Locate every blood parasite and identify its species.
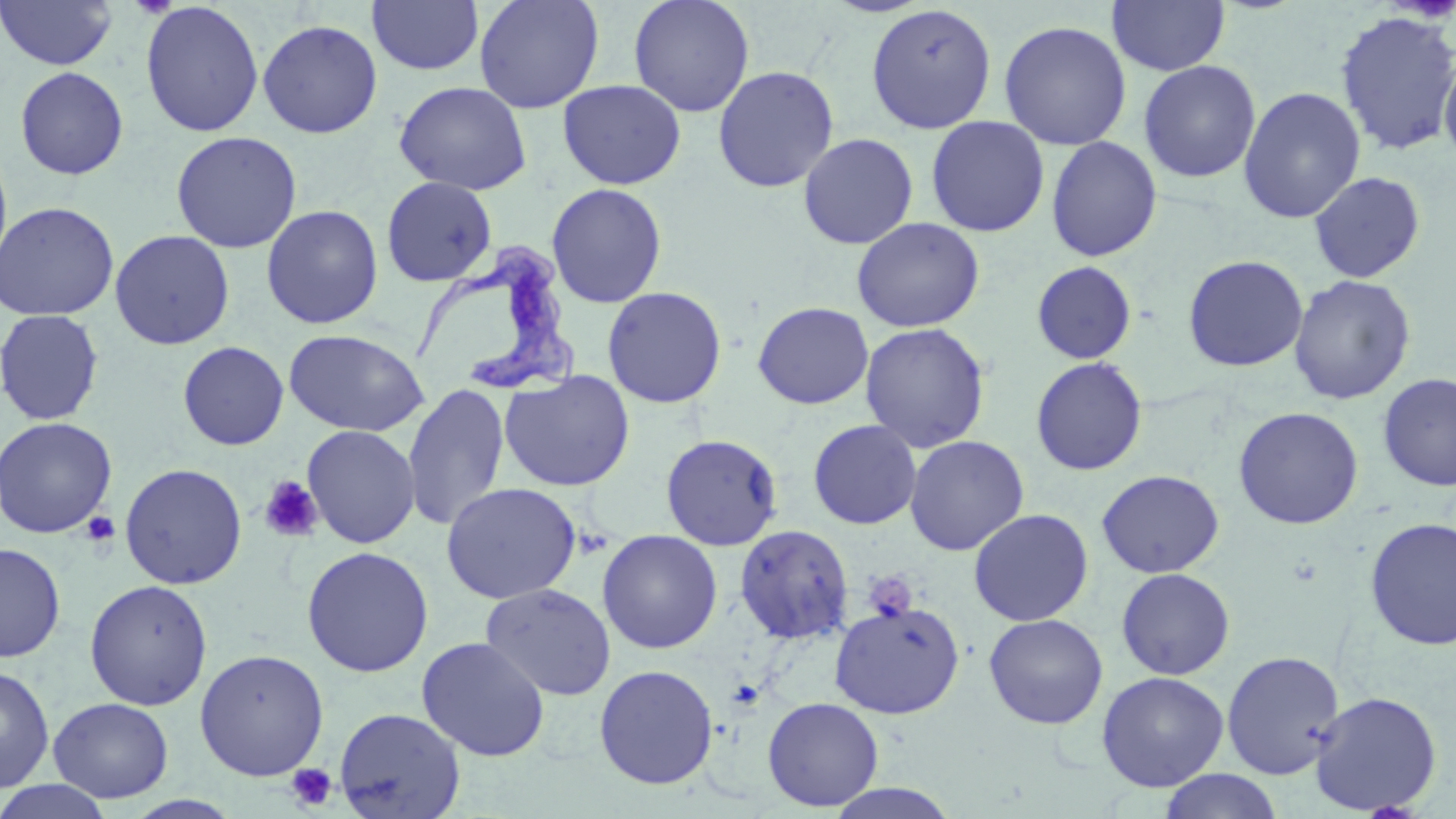
Approximate bounding boxes as (x1,y1)-(x2,y2) corner pairs in pixels.
Trypanosoma brucei: (406,236)-(576,396).
No Plasmodium falciparum, Plasmodium ovale, Plasmodium malariae, Plasmodium vivax, or Babesia divergens observed.

slide-level diagnosis = Trypanosoma brucei
preparation = thin blood film
stain = May-Grünwald-Giemsa
uninfected red blood cell locations = approximate bounding boxes as (x1,y1)-(x2,y2) corner pairs in pixels: (366,0)-(484,76), (474,0)-(604,114), (629,0)-(755,117), (1107,0)-(1231,77), (0,1)-(117,71), (139,1)-(264,138), (865,3)-(998,134), (1334,11)-(1456,155), (257,18)-(383,139), (998,19)-(1132,151), (1439,51)-(1456,166), (1138,60)-(1261,183), (712,65)-(840,193), (14,66)-(129,180), (557,79)-(686,190), (393,81)-(532,195), (1238,86)-(1365,223), (925,116)-(1050,237), (170,131)-(303,253), (798,132)-(919,250), (1046,136)-(1162,262), (0,143)-(13,276), (1309,171)-(1426,284), (381,176)-(498,286), (546,182)-(668,308), (0,200)-(119,322), (261,204)-(384,329), (851,217)-(985,333), (109,229)-(235,350), (1182,254)-(1308,373), (1031,261)-(1136,364), (1289,274)-(1416,405), (601,286)-(728,409), (752,301)-(874,410), (0,309)-(105,426), (859,322)-(990,453), (283,329)-(430,437), (178,341)-(289,450), (1030,357)-(1148,475), (498,370)-(635,491), (1377,372)-(1456,491), (402,383)-(510,531), (1233,406)-(1364,530), (0,416)-(117,538), (807,419)-(922,530), (301,424)-(421,548), (660,433)-(783,550), (904,435)-(1029,555), (119,462)-(248,590), (1097,469)-(1224,579), (440,482)-(582,604), (968,508)-(1093,627), (1364,517)-(1456,650), (734,524)-(854,644), (597,529)-(722,654), (0,542)-(66,662), (301,545)-(434,677), (1116,568)-(1235,680), (84,579)-(212,711), (480,583)-(616,701), (829,600)-(965,719), (983,613)-(1108,730), (416,636)-(550,762), (194,648)-(329,781), (1221,650)-(1345,779), (0,664)-(55,793), (593,664)-(719,790), (1096,671)-(1229,792), (1309,691)-(1442,816), (762,696)-(884,811), (48,697)-(173,803), (334,707)-(466,819), (1158,769)-(1284,819), (0,780)-(114,819), (821,783)-(963,819)
image size = 1456×819 pixels
magnification = 1000x
platelet locations = approximate bounding boxes as (x1,y1)-(x2,y2) corner pairs in pixels: (258,476)-(324,543), (81,511)-(120,548), (863,570)-(917,623), (286,764)-(337,810)
modality = light microscopy
field of view = single